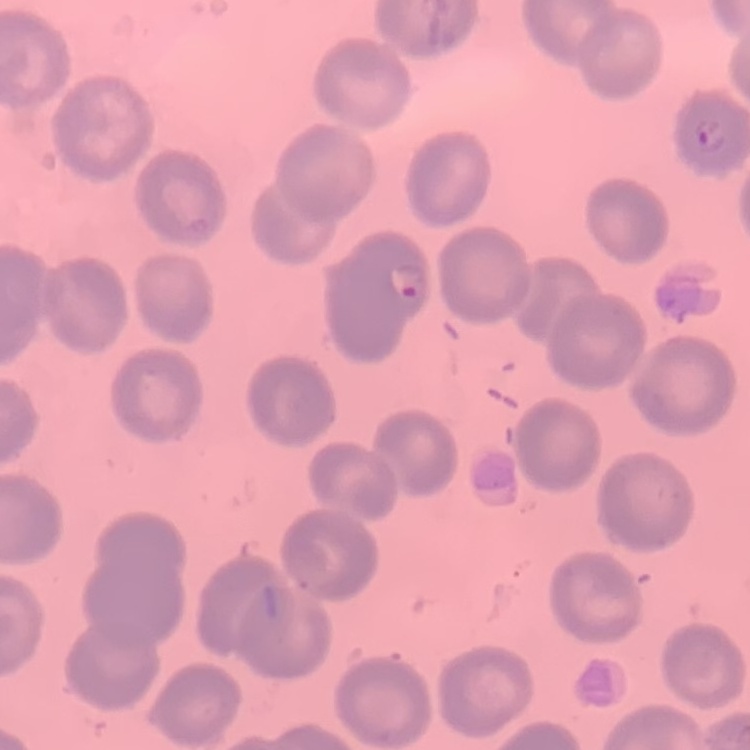
The erythrocytes show no rouleaux formation. Field's or Giemsa stain. Thin blood film. Square crop of a larger photomicrograph.